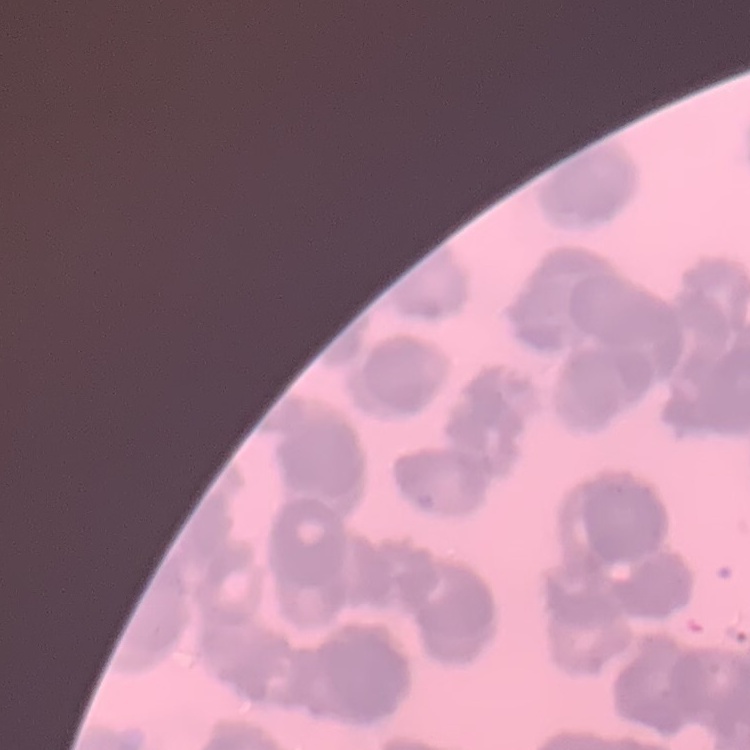

The erythrocytes exhibit rouleaux formation. Field's or Giemsa stain. One tile cut from a larger photomicrograph. Thin peripheral smear.